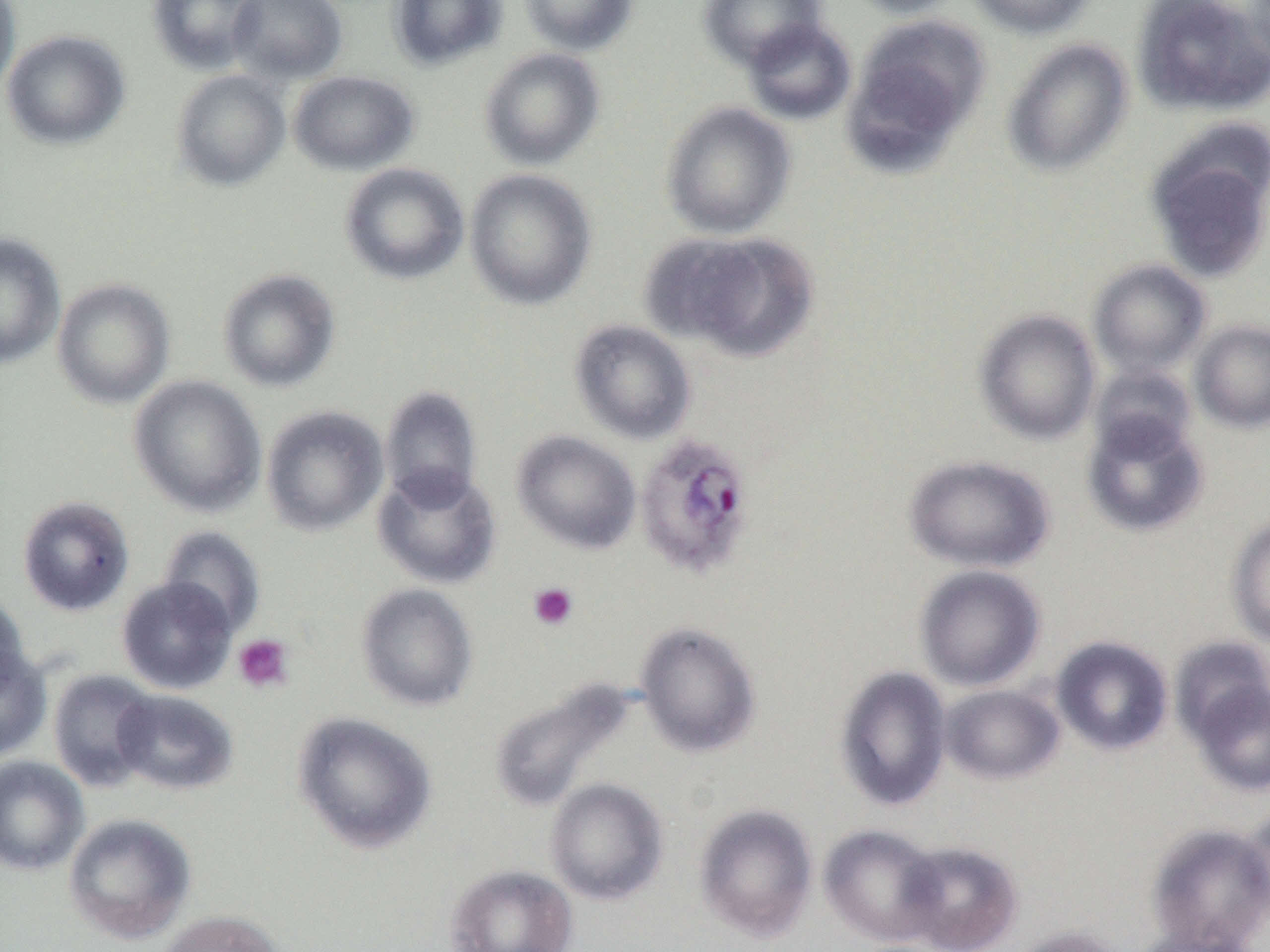

Summary:
  - Coordinate format: approximate bounding boxes as [x1, y1, x2, y2] in pixels
  - Uninfected red blood cell locations: [146, 0, 264, 75], [227, 0, 348, 85], [387, 0, 508, 71], [517, 0, 639, 57], [698, 0, 826, 70], [844, 0, 968, 18], [967, 0, 1097, 39], [1132, 0, 1270, 116], [0, 2, 21, 101], [845, 15, 989, 165], [742, 19, 856, 125], [1, 30, 131, 151], [1001, 38, 1134, 177], [479, 48, 606, 171], [171, 69, 291, 192], [288, 70, 420, 176], [659, 101, 796, 239], [1147, 151, 1270, 282], [339, 162, 470, 285], [464, 168, 598, 311], [651, 230, 819, 362], [0, 233, 66, 369], [1088, 259, 1212, 378], [217, 268, 341, 393], [52, 278, 175, 409], [974, 308, 1101, 445], [568, 319, 697, 445], [1190, 320, 1270, 434], [1089, 364, 1197, 460], [128, 375, 267, 517], [380, 386, 483, 507], [260, 405, 389, 536], [1081, 411, 1210, 538], [511, 430, 641, 554], [903, 454, 1056, 573], [372, 465, 502, 589], [16, 495, 135, 616], [1227, 514, 1270, 649], [158, 525, 266, 636], [914, 564, 1046, 692], [116, 577, 237, 694], [356, 583, 479, 712], [0, 590, 29, 698], [634, 620, 762, 759], [1051, 636, 1173, 755], [1168, 636, 1270, 748], [0, 643, 52, 761], [834, 664, 952, 812], [48, 669, 159, 792], [1187, 673, 1269, 798], [488, 678, 636, 814], [940, 684, 1065, 785], [112, 689, 238, 796], [292, 711, 437, 854], [0, 755, 89, 876], [545, 778, 669, 905], [694, 803, 818, 942], [1239, 803, 1270, 919], [63, 812, 197, 944], [1145, 823, 1270, 952], [819, 824, 945, 946], [897, 839, 1022, 952], [445, 863, 579, 952], [157, 909, 284, 952], [1007, 925, 1126, 952], [1128, 925, 1263, 952]
  - Plasmodium ovale-infected red blood cell locations: [633, 433, 756, 580]
  - Platelet locations: [528, 582, 579, 631], [232, 633, 295, 694]
  - Slide-level diagnosis: Plasmodium ovale
  - Magnification: 1000x
  - Field of view: one of a larger specimen
  - Modality: light microscopy
  - Preparation: thin blood smear
  - Image size: 1270×952 pixels